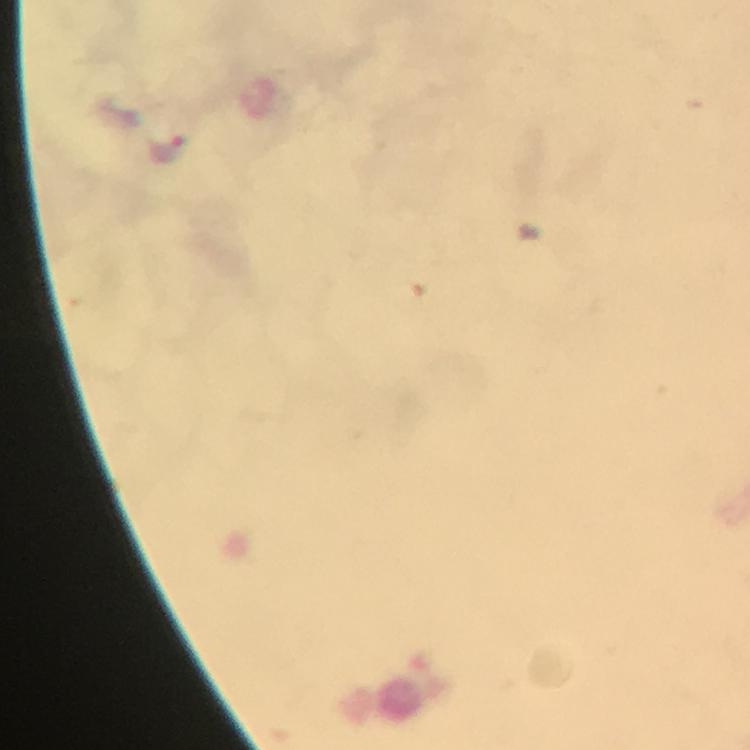

magnification = 100x
capture = smartphone photograph through a microscope
image size = 750×750 pixels
stain = Giemsa
preparation = thick smear
cropped from = a single field of view
malaria parasite locations = approximate centers as (x, y) in pixels: (167, 146)
context = from a diagnostic examination for malaria
immersion oil = applied